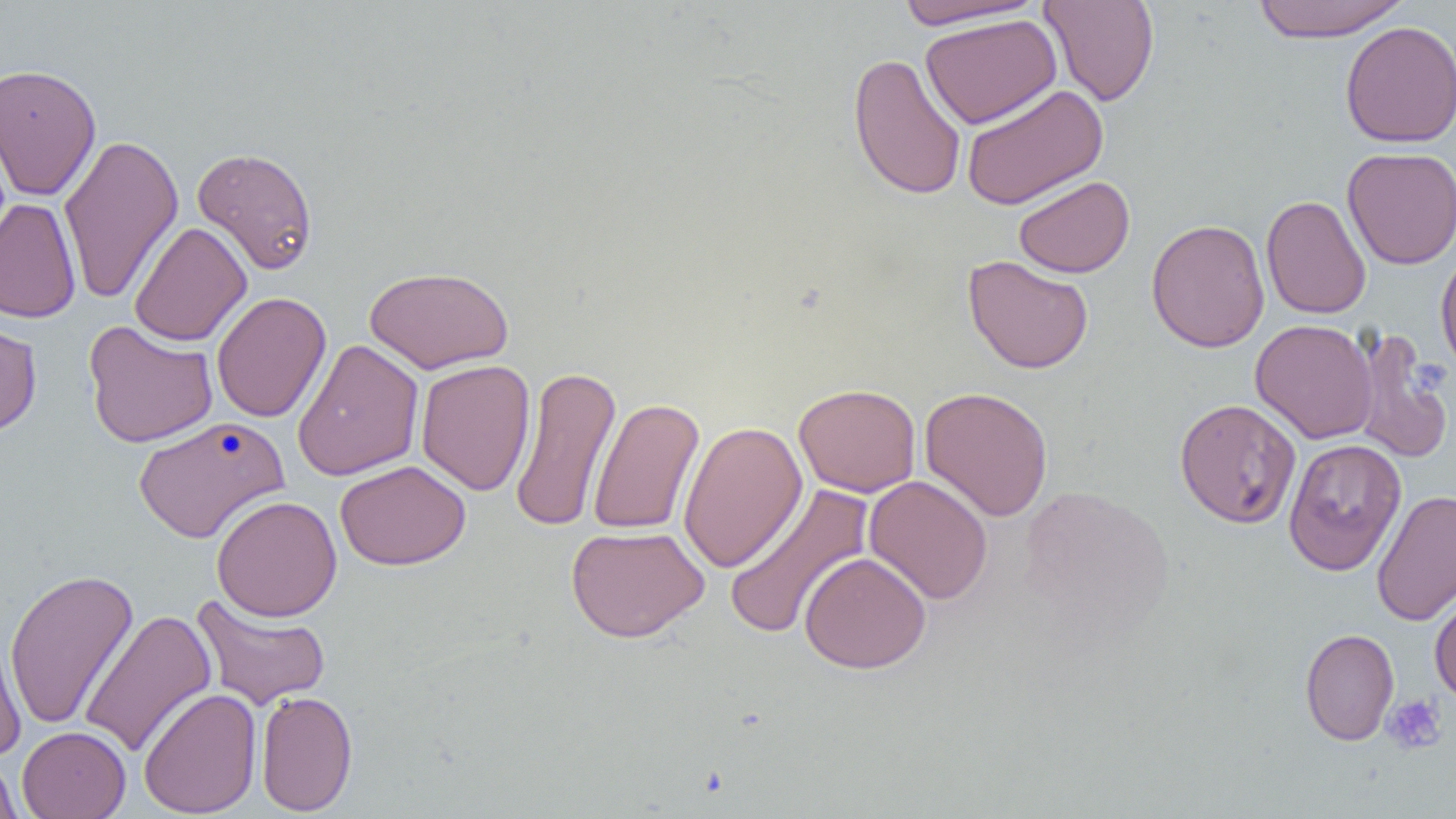

{
  "slide_level_diagnosis": "negative for blood parasites",
  "modality": "light microscopy",
  "field_of_view": "one of a larger specimen",
  "magnification": "1000x",
  "uninfected_red_blood_cell_locations": "approximate bounding boxes as (x1,y1)-(x2,y2) corner pairs in pixels: (894,0)-(1047,32), (1040,0)-(1160,107), (1251,0)-(1410,44), (920,14)-(1062,129), (1339,20)-(1456,148), (847,52)-(967,201), (0,63)-(102,201), (960,83)-(1108,211), (59,133)-(183,306), (192,146)-(319,275), (1342,147)-(1456,270), (1014,174)-(1135,278), (1261,194)-(1372,319), (0,197)-(81,323), (1146,218)-(1270,353), (130,221)-(251,346), (1435,245)-(1456,376), (963,254)-(1094,375), (363,265)-(514,374), (211,292)-(331,423), (0,318)-(42,437), (1250,319)-(1379,444), (1271,319)-(1388,575), (82,320)-(218,448), (1350,329)-(1452,465), (292,339)-(424,481), (415,359)-(535,496), (509,365)-(622,533), (794,383)-(921,498), (919,386)-(1054,522), (588,397)-(704,535), (1174,397)-(1301,529), (133,415)-(290,543), (678,420)-(807,573), (1283,437)-(1407,575), (335,460)-(471,571), (864,474)-(993,605), (723,482)-(875,641), (1372,489)-(1456,627), (212,494)-(342,622), (566,525)-(709,643), (799,551)-(931,674), (4,569)-(139,730), (1429,587)-(1456,707), (189,593)-(331,711), (80,609)-(217,758), (0,617)-(26,763), (1299,628)-(1399,745), (138,688)-(262,817), (256,690)-(358,816), (17,726)-(131,819), (1,751)-(23,819)",
  "preparation": "thin blood film",
  "platelet_locations": "approximate bounding boxes as (x1,y1)-(x2,y2) corner pairs in pixels: (1381,694)-(1448,755)",
  "image_size": "1456×819 pixels"
}